Outline each blood parasite and name the species.
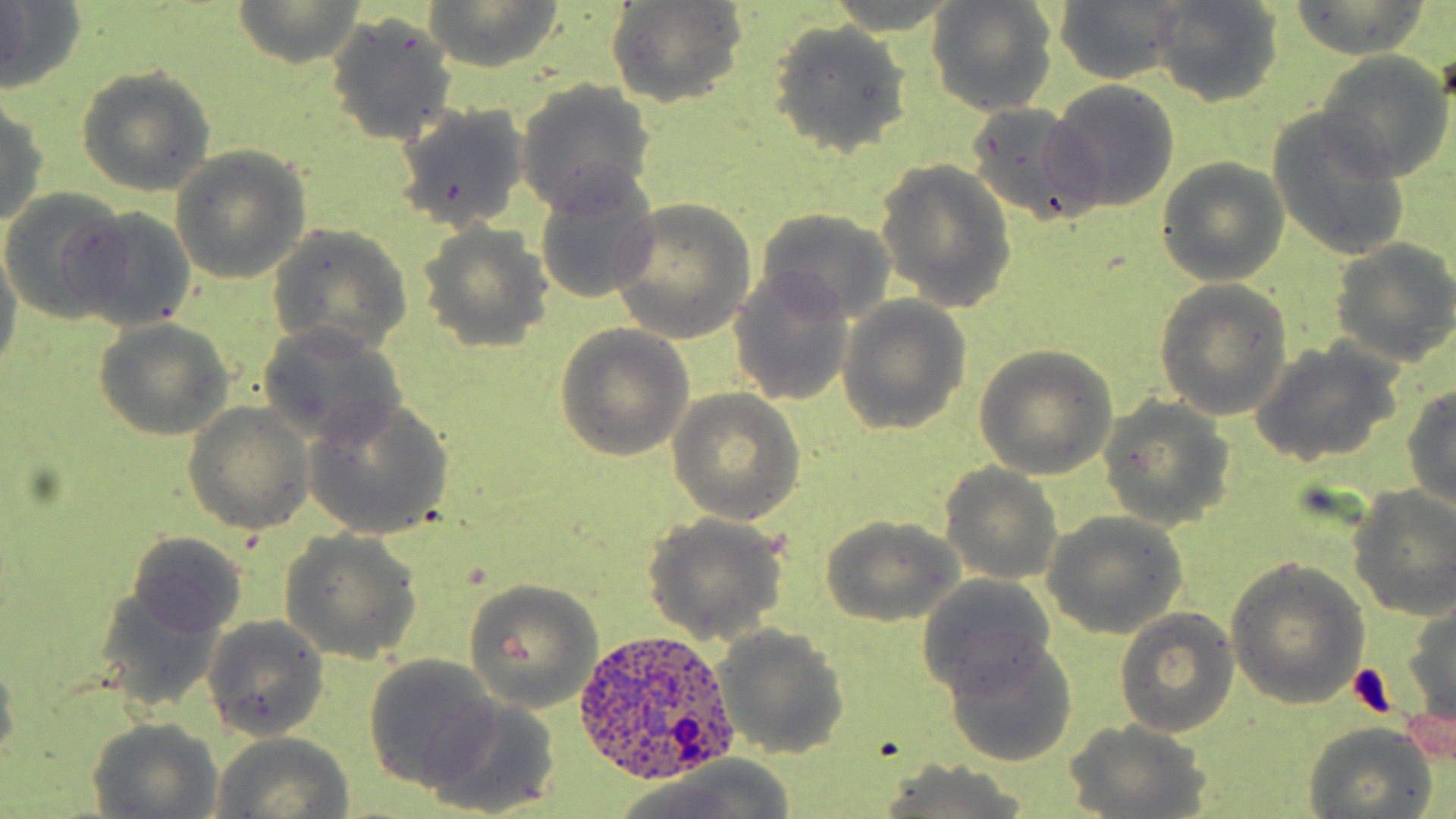

Approximate bounding boxes as [x1, y1, x2, y2] in pixels.
Plasmodium ovale-infected red blood cells: [576, 629, 737, 785].
No Plasmodium falciparum, Plasmodium malariae, Plasmodium vivax, Babesia divergens, or Trypanosoma brucei observed.

{
  "slide_level_diagnosis": "Plasmodium ovale",
  "field_of_view": "single",
  "preparation": "thin blood film",
  "stain": "May-Grünwald-Giemsa",
  "modality": "light microscopy",
  "platelet_locations": "approximate bounding boxes as [x1, y1, x2, y2] in pixels: [1348, 662, 1399, 717]",
  "magnification": "1000x",
  "image_size": "1456×819 pixels",
  "uninfected_red_blood_cell_locations": "approximate bounding boxes as [x1, y1, x2, y2] in pixels: [0, 0, 86, 94], [423, 0, 563, 71], [1051, 0, 1187, 86], [230, 1, 371, 70], [606, 1, 750, 109], [923, 1, 1061, 116], [1148, 1, 1286, 107], [1284, 1, 1434, 60], [323, 11, 459, 146], [768, 19, 915, 158], [1314, 50, 1454, 180], [76, 66, 218, 197], [513, 78, 657, 215], [1046, 79, 1181, 213], [0, 99, 48, 226], [963, 102, 1103, 230], [389, 103, 532, 236], [1264, 108, 1417, 264], [170, 145, 313, 284], [1155, 158, 1291, 286], [873, 160, 1019, 313], [529, 170, 661, 308], [0, 188, 128, 325], [607, 199, 756, 344], [751, 207, 900, 324], [66, 208, 199, 333], [415, 222, 555, 353], [267, 225, 414, 355], [1328, 238, 1456, 367], [0, 239, 22, 383], [727, 266, 858, 408], [1154, 280, 1293, 420], [835, 294, 971, 434], [90, 318, 234, 441], [256, 323, 409, 448], [555, 324, 695, 460], [1247, 339, 1405, 467], [973, 346, 1119, 479], [1400, 384, 1456, 510], [667, 389, 807, 525], [1099, 397, 1237, 529], [300, 399, 454, 541], [182, 401, 316, 535], [938, 464, 1064, 584], [1346, 485, 1456, 620], [1041, 511, 1189, 638], [640, 512, 791, 646], [817, 515, 968, 626], [279, 528, 424, 667], [124, 531, 249, 639], [1225, 559, 1371, 709], [916, 574, 1060, 697], [462, 579, 605, 713], [93, 584, 223, 710], [1403, 595, 1456, 734], [1114, 608, 1239, 739], [202, 616, 331, 741], [712, 625, 850, 758], [942, 641, 1079, 767], [0, 648, 20, 761], [361, 654, 501, 790], [428, 698, 560, 816], [87, 718, 224, 816], [1065, 720, 1213, 817], [1301, 723, 1437, 818], [208, 732, 354, 819], [870, 760, 1039, 819], [599, 768, 797, 819]"
}